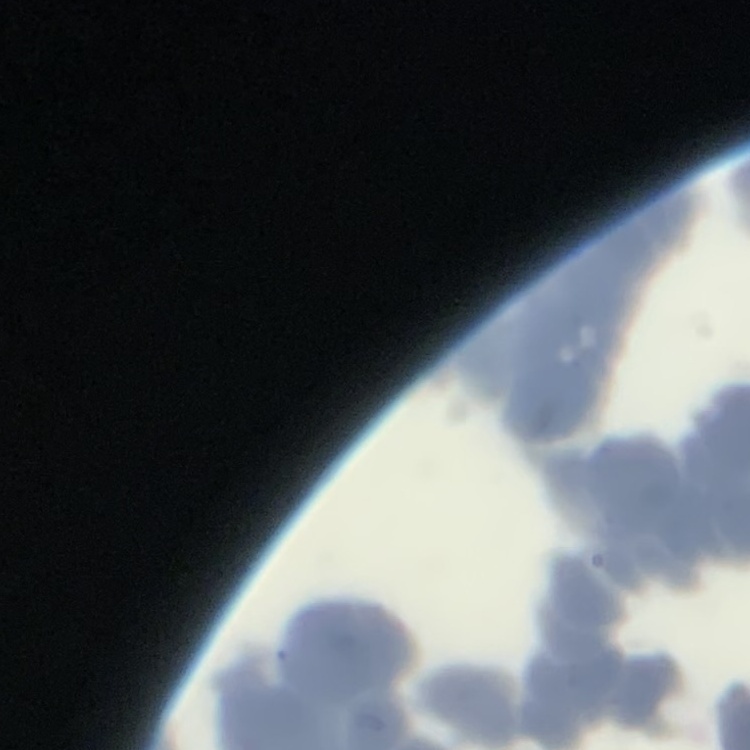

The erythrocytes exhibit rouleaux formation. Thin blood smear. One tile cut from a larger photomicrograph. Stained with either Field's or Giemsa.